Locate every malaria parasite.
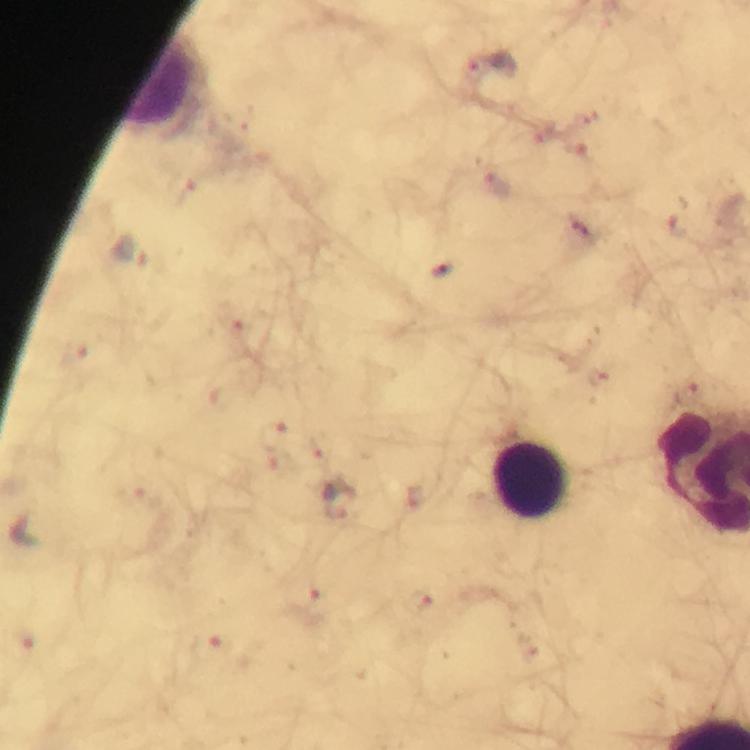
Approximate centers as (x, y) in pixels.
Malaria parasites: (487, 64), (545, 133), (498, 184), (675, 224), (581, 226), (131, 254), (442, 271), (235, 321), (75, 356), (599, 380), (691, 395), (273, 438), (421, 596), (306, 600), (212, 646).

Summary:
  - Leukocyte locations: (158, 82), (534, 482)
  - Context: from a diagnostic examination for malaria
  - Magnification: 100x
  - Image size: 750×750 pixels
  - Stain: Giemsa
  - Cropped from: a single field of view
  - Immersion oil: applied
  - Capture: smartphone photograph through a microscope
  - Preparation: thick blood film